State the blood parasite species.
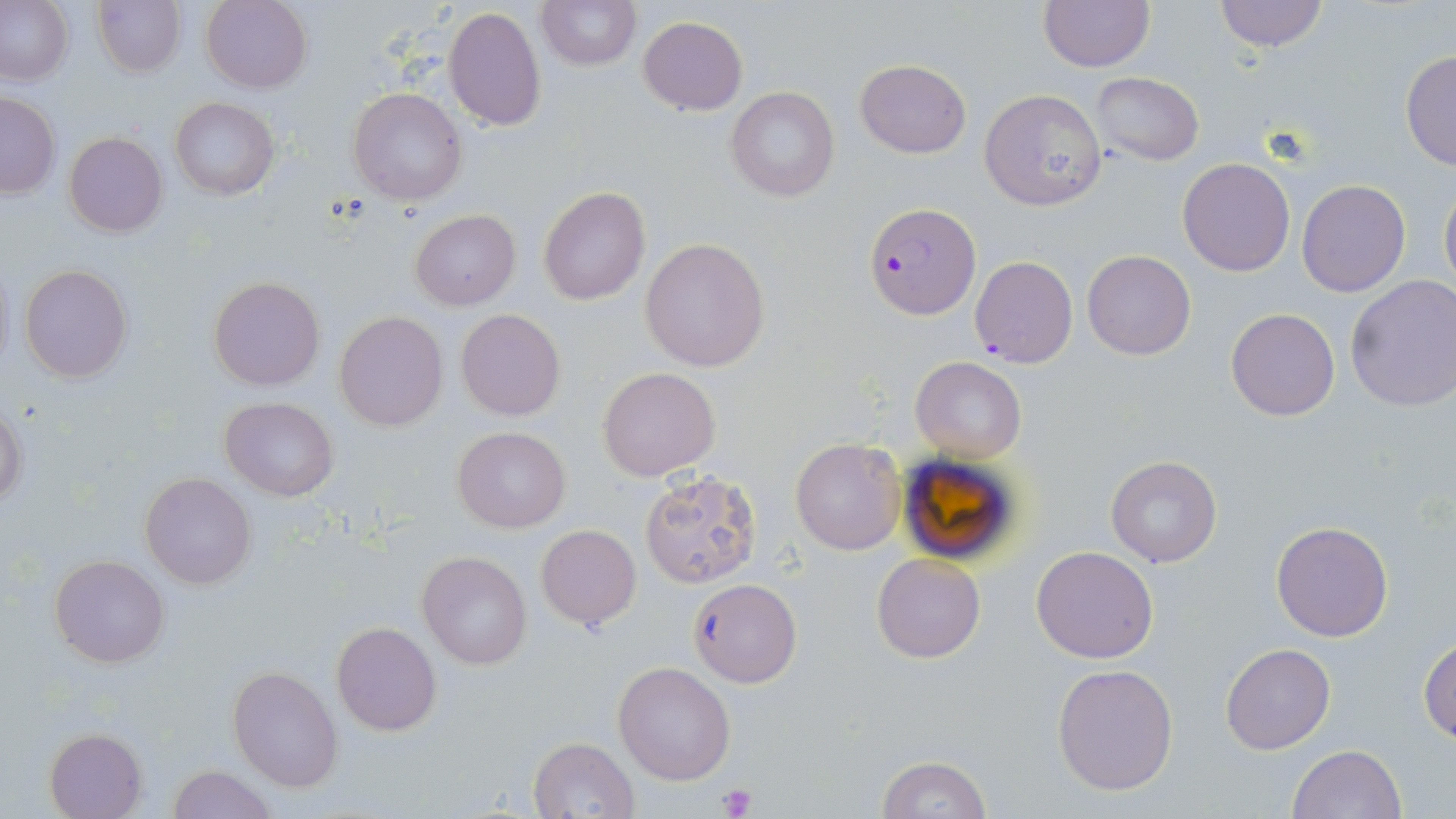

Plasmodium falciparum.

Summary:
  - Coordinate format: approximate bounding boxes as named x1/y1/x2/y2 corners in pixels
  - Uninfected red blood cell locations: (x1=92, y1=0, x2=185, y2=76), (x1=200, y1=0, x2=312, y2=93), (x1=536, y1=0, x2=640, y2=72), (x1=1212, y1=0, x2=1328, y2=51), (x1=0, y1=1, x2=73, y2=86), (x1=1037, y1=1, x2=1155, y2=71), (x1=443, y1=5, x2=548, y2=133), (x1=638, y1=15, x2=747, y2=115), (x1=1400, y1=50, x2=1455, y2=171), (x1=855, y1=59, x2=971, y2=158), (x1=1090, y1=72, x2=1204, y2=164), (x1=347, y1=87, x2=467, y2=205), (x1=725, y1=87, x2=841, y2=203), (x1=978, y1=89, x2=1108, y2=211), (x1=0, y1=93, x2=61, y2=198), (x1=170, y1=97, x2=279, y2=200), (x1=64, y1=132, x2=169, y2=238), (x1=1177, y1=157, x2=1295, y2=276), (x1=1296, y1=179, x2=1410, y2=297), (x1=1439, y1=179, x2=1456, y2=295), (x1=536, y1=184, x2=651, y2=306), (x1=410, y1=209, x2=521, y2=311), (x1=639, y1=237, x2=770, y2=372), (x1=1081, y1=249, x2=1196, y2=360), (x1=19, y1=263, x2=133, y2=384), (x1=1344, y1=275, x2=1456, y2=413), (x1=208, y1=276, x2=325, y2=391), (x1=1226, y1=307, x2=1340, y2=421), (x1=456, y1=310, x2=566, y2=422), (x1=335, y1=312, x2=449, y2=431), (x1=909, y1=357, x2=1027, y2=461), (x1=597, y1=366, x2=721, y2=481), (x1=219, y1=398, x2=338, y2=501), (x1=0, y1=403, x2=27, y2=510), (x1=453, y1=427, x2=571, y2=531), (x1=790, y1=438, x2=906, y2=554), (x1=1105, y1=457, x2=1222, y2=568), (x1=637, y1=470, x2=762, y2=588), (x1=139, y1=472, x2=257, y2=590), (x1=1271, y1=520, x2=1394, y2=641), (x1=536, y1=525, x2=641, y2=630), (x1=1030, y1=546, x2=1159, y2=664), (x1=418, y1=550, x2=532, y2=670), (x1=872, y1=553, x2=986, y2=663), (x1=49, y1=554, x2=169, y2=668), (x1=688, y1=577, x2=801, y2=688), (x1=331, y1=621, x2=442, y2=736), (x1=1419, y1=636, x2=1456, y2=742), (x1=1220, y1=644, x2=1336, y2=754), (x1=613, y1=661, x2=735, y2=785), (x1=1052, y1=663, x2=1179, y2=796), (x1=227, y1=665, x2=342, y2=791), (x1=45, y1=728, x2=147, y2=818), (x1=527, y1=736, x2=640, y2=819), (x1=1286, y1=745, x2=1405, y2=819), (x1=875, y1=754, x2=991, y2=818), (x1=167, y1=764, x2=280, y2=818)
  - Plasmodium falciparum-infected red blood cell locations: (x1=865, y1=203, x2=981, y2=319), (x1=970, y1=254, x2=1078, y2=369)
  - Platelet locations: (x1=718, y1=783, x2=757, y2=817)
  - Modality: light microscopy
  - Magnification: 1000x
  - Stain: May-Grünwald-Giemsa
  - Preparation: thin blood film
  - Image size: 1456×819 pixels
  - Field of view: single